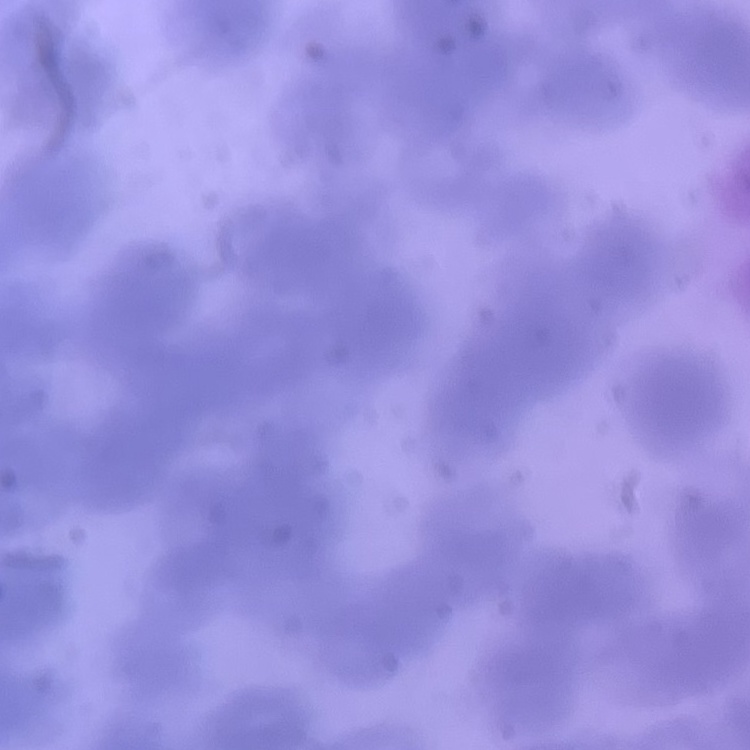 The erythrocytes exhibit rouleaux formation. Field's or Giemsa stain. Thin blood smear. One tile cut from a larger photomicrograph.